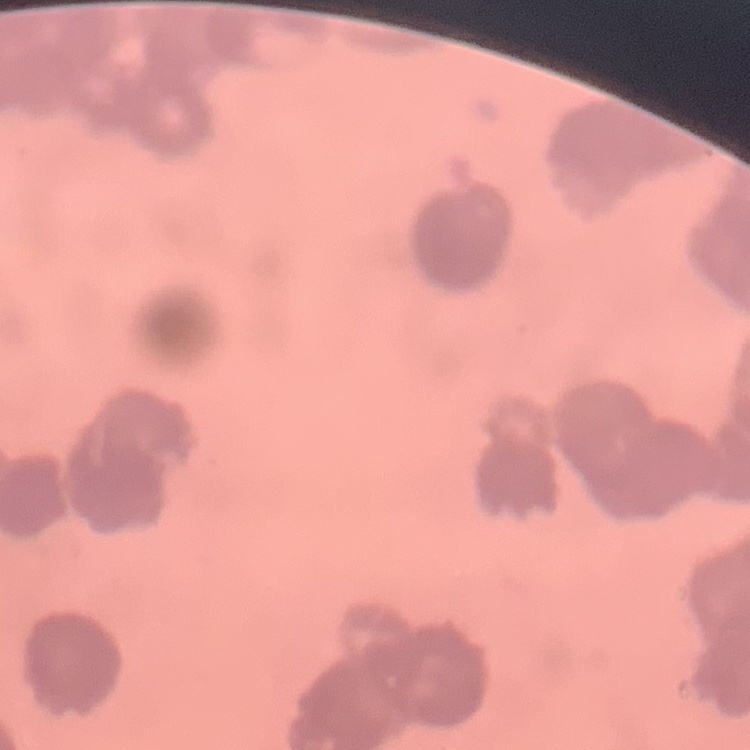

The red blood cells show rouleaux formation. Stained with either Field's or Giemsa. Square crop of a larger photomicrograph. Thin peripheral smear.